Name the blood parasite species.
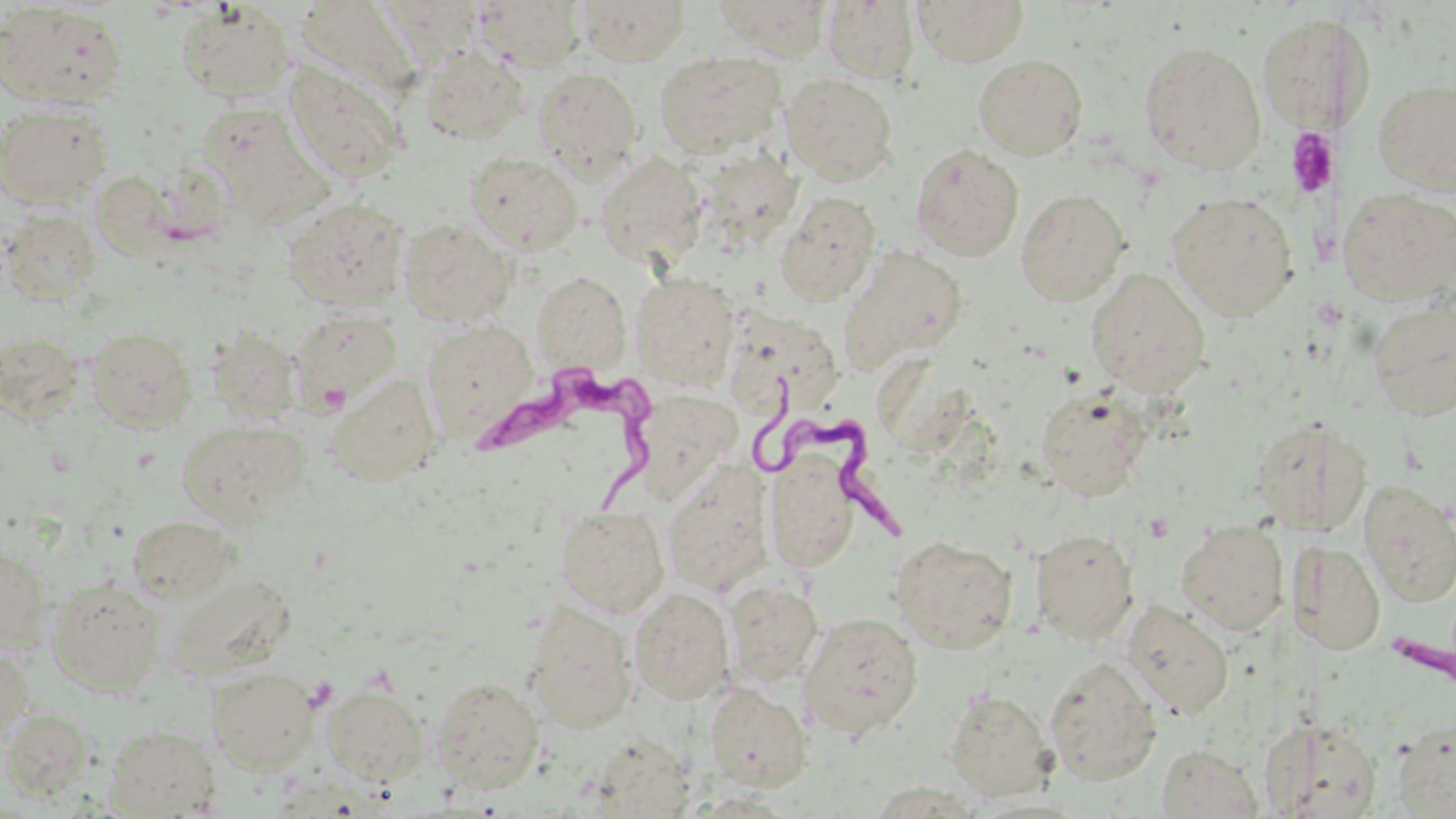

Trypanosoma brucei.

magnification: 1000x
trypanosoma_brucei_locations: 'approximate bounding boxes as (x1,y1)-(x2,y2) corner pairs in pixels: (465,358)-(660,519), (760,380)-(910,552), (1392,625)-(1456,707)'
preparation: thin blood smear
platelet_locations: 'approximate bounding boxes as (x1,y1)-(x2,y2) corner pairs in pixels: (1286,128)-(1339,197)'
modality: optical microscopy
uninfected_red_blood_cell_locations: 'approximate bounding boxes as (x1,y1)-(x2,y2) corner pairs in pixels: (376,0)-(487,65), (577,0)-(691,65), (713,0)-(836,61), (912,0)-(1030,66), (295,1)-(420,97), (473,1)-(587,71), (822,1)-(921,84), (177,2)-(295,103), (0,4)-(127,108), (1258,13)-(1375,131), (1139,41)-(1265,173), (420,46)-(528,144), (654,53)-(786,157), (973,54)-(1088,160), (283,60)-(406,184), (533,67)-(643,182), (782,73)-(898,185), (1373,78)-(1456,195), (200,101)-(329,223), (0,102)-(113,208), (911,144)-(1024,260), (465,151)-(583,254), (596,152)-(707,268), (91,171)-(177,260), (1337,188)-(1455,307), (1016,189)-(1130,305), (775,191)-(881,306), (1167,192)-(1297,320), (282,196)-(410,310), (2,207)-(101,305), (399,218)-(516,326), (836,244)-(968,375), (1086,268)-(1210,397), (533,271)-(630,373), (631,273)-(739,388), (1367,297)-(1456,421), (731,306)-(862,428), (288,308)-(402,414), (424,318)-(538,443), (206,323)-(304,426), (87,326)-(197,433), (0,331)-(84,424), (326,373)-(442,486), (1036,386)-(1151,500), (637,391)-(741,503), (1251,416)-(1371,535), (177,419)-(310,525), (765,454)-(859,573), (661,460)-(777,598), (1360,481)-(1456,606), (555,507)-(669,618), (128,515)-(238,605), (1176,519)-(1289,635), (1030,528)-(1139,643), (890,535)-(1019,653), (1291,541)-(1386,655), (0,548)-(53,652), (47,577)-(166,695), (724,579)-(823,687), (629,587)-(734,704), (1123,600)-(1234,720), (525,602)-(637,733), (798,612)-(922,738), (0,645)-(32,745), (1043,656)-(1162,785), (207,665)-(319,775), (431,676)-(544,792), (704,683)-(812,792), (322,684)-(429,785), (944,688)-(1057,800), (1,708)-(95,799), (1260,715)-(1383,818), (1393,718)-(1456,816), (104,724)-(221,817), (1157,744)-(1264,818)'
stain: May-Grünwald-Giemsa
field_of_view: single
image_size: 1456×819 pixels